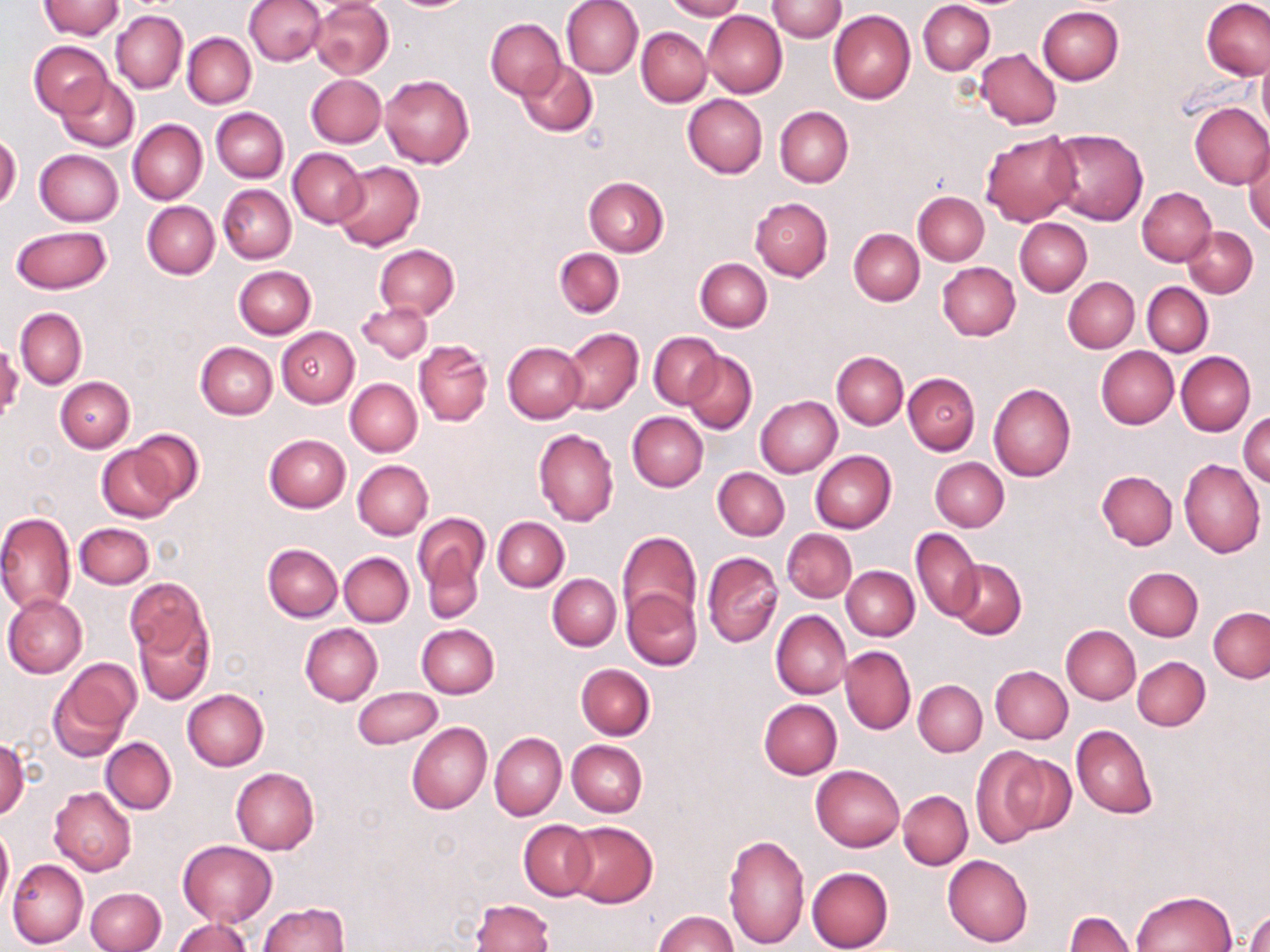
Approximate bounding boxes as [x1, y1, x2, y2] in pixels. Uninfected red blood cell locations: [244, 0, 326, 66], [561, 0, 644, 78], [663, 0, 744, 20], [768, 0, 845, 43], [918, 0, 995, 76], [1200, 0, 1270, 81], [38, 1, 125, 40], [310, 1, 393, 79], [1038, 6, 1124, 84], [111, 10, 187, 93], [702, 10, 787, 98], [829, 11, 915, 104], [486, 19, 566, 98], [636, 27, 711, 107], [182, 33, 256, 108], [30, 42, 112, 119], [976, 48, 1061, 129], [1258, 50, 1270, 142], [515, 60, 597, 136], [306, 73, 385, 148], [56, 74, 139, 152], [380, 75, 474, 168], [683, 94, 768, 178], [1188, 101, 1270, 189], [774, 107, 853, 188], [211, 108, 288, 183], [128, 119, 207, 205], [1048, 128, 1148, 225], [980, 131, 1082, 226], [0, 132, 21, 212], [1244, 139, 1270, 235], [287, 148, 366, 226], [35, 149, 124, 226], [332, 161, 425, 251], [583, 177, 669, 256], [218, 184, 296, 264], [1137, 186, 1217, 265], [913, 191, 989, 265], [750, 197, 832, 281], [142, 202, 219, 280], [1015, 218, 1092, 296], [11, 226, 110, 295], [1182, 226, 1258, 297], [849, 228, 924, 305], [374, 244, 458, 319], [554, 248, 624, 316], [695, 258, 772, 331], [937, 262, 1020, 341], [233, 265, 316, 338], [1063, 277, 1139, 353], [1143, 283, 1213, 356], [357, 302, 432, 361], [15, 308, 87, 388], [276, 327, 359, 407], [562, 327, 643, 415], [649, 332, 723, 408], [414, 340, 492, 426], [196, 341, 277, 419], [503, 341, 587, 423], [1096, 346, 1178, 429], [684, 351, 757, 434], [1176, 351, 1255, 436], [831, 352, 908, 430], [903, 373, 980, 454], [55, 377, 135, 453], [345, 378, 422, 457], [989, 383, 1076, 482], [755, 396, 841, 477], [627, 411, 707, 491], [1238, 412, 1270, 485], [128, 429, 204, 505], [533, 429, 618, 527], [264, 433, 350, 512], [97, 444, 180, 523], [811, 451, 896, 533], [931, 457, 1009, 532], [1178, 458, 1266, 557], [353, 460, 433, 539], [713, 467, 789, 540], [1096, 470, 1177, 550], [0, 510, 76, 615], [413, 513, 487, 592], [493, 517, 569, 591], [76, 522, 154, 588], [911, 528, 983, 620], [782, 529, 857, 603], [616, 530, 701, 629], [263, 544, 342, 622], [424, 551, 483, 623], [702, 551, 782, 647], [339, 553, 413, 627], [949, 559, 1026, 638], [841, 566, 919, 641], [1123, 567, 1203, 641], [548, 574, 621, 650], [125, 577, 210, 668], [622, 589, 702, 672], [3, 594, 88, 677], [132, 604, 215, 704], [14, 607, 106, 723], [1208, 607, 1269, 683], [772, 610, 851, 699], [300, 623, 383, 705], [416, 624, 498, 698], [1061, 625, 1140, 704], [840, 645, 916, 735], [1132, 656, 1210, 731], [576, 663, 654, 740], [48, 665, 137, 761], [990, 665, 1073, 743], [913, 680, 987, 756], [352, 686, 442, 750], [183, 687, 269, 770], [758, 699, 841, 778], [407, 721, 491, 814], [1072, 724, 1158, 819], [489, 731, 566, 820], [101, 736, 176, 813], [0, 739, 29, 820], [568, 740, 647, 817], [971, 745, 1051, 848], [997, 752, 1078, 836], [811, 764, 904, 850], [230, 766, 319, 854], [49, 786, 135, 875], [898, 791, 972, 869], [518, 819, 596, 899], [563, 820, 658, 908], [0, 825, 13, 912], [724, 834, 810, 950], [179, 840, 277, 927], [942, 854, 1033, 946], [7, 859, 88, 948], [806, 866, 894, 952], [85, 887, 166, 952], [1130, 890, 1238, 952], [471, 899, 555, 952], [257, 902, 350, 952], [1244, 909, 1269, 952], [655, 910, 738, 952], [1065, 912, 1135, 952], [173, 917, 251, 952]. Slide-level diagnosis: negative for blood parasites. Captured at 1000x magnification. Light microscopy. Image is 1270×952 pixels. Thin blood smear. Single field of view. May-Grünwald-Giemsa stain.